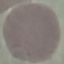

Summary:
  - Result: negative for malaria parasites
  - Stain: Giemsa
  - Capture: smartphone through the microscope eyepiece
  - Preparation: thin blood smear
  - Image type: automatically extracted cell patch, resized to 64 × 64 pixels